Name the parasite shown.
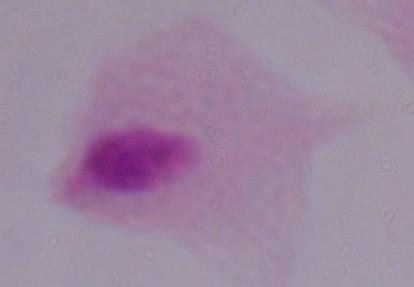

A trichomonad.

Summary:
  - Modality: micrograph
  - Magnification: 1000x